Name the parasite shown.
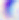

This is Toxoplasma gondii.

Photomicrograph. 400x magnification.